Locate every blood parasite and identify its species.
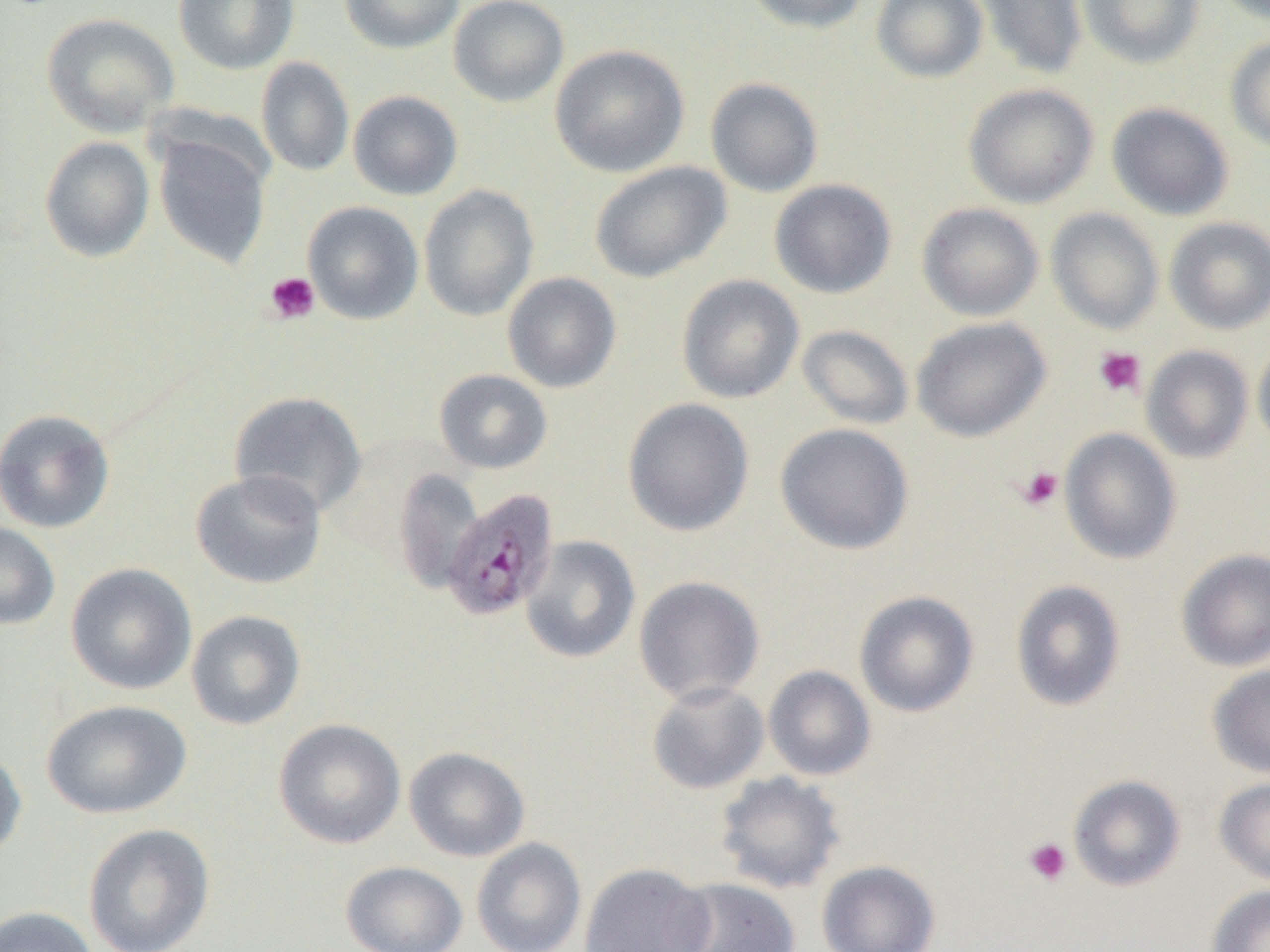

Approximate bounding boxes as named x1/y1/x2/y2 corners in pixels.
Plasmodium malariae-infected red blood cells: (x1=440, y1=487, x2=559, y2=622).
No Plasmodium falciparum, Plasmodium ovale, Plasmodium vivax, Babesia divergens, or Trypanosoma brucei observed.

Summary:
  - Uninfected red blood cell locations: (x1=173, y1=0, x2=299, y2=74), (x1=340, y1=0, x2=465, y2=54), (x1=448, y1=0, x2=569, y2=107), (x1=741, y1=0, x2=869, y2=34), (x1=871, y1=0, x2=988, y2=83), (x1=974, y1=0, x2=1089, y2=80), (x1=1078, y1=0, x2=1205, y2=68), (x1=1211, y1=0, x2=1269, y2=25), (x1=41, y1=12, x2=180, y2=137), (x1=1225, y1=36, x2=1270, y2=153), (x1=550, y1=44, x2=690, y2=178), (x1=256, y1=57, x2=355, y2=177), (x1=705, y1=77, x2=824, y2=198), (x1=963, y1=83, x2=1099, y2=209), (x1=348, y1=90, x2=463, y2=200), (x1=1106, y1=102, x2=1234, y2=221), (x1=153, y1=133, x2=271, y2=270), (x1=39, y1=136, x2=155, y2=263), (x1=589, y1=161, x2=732, y2=283), (x1=769, y1=179, x2=897, y2=299), (x1=419, y1=184, x2=539, y2=321), (x1=303, y1=201, x2=424, y2=325), (x1=917, y1=202, x2=1044, y2=321), (x1=1045, y1=208, x2=1164, y2=334), (x1=1164, y1=217, x2=1270, y2=334), (x1=502, y1=272, x2=622, y2=393), (x1=676, y1=274, x2=805, y2=404), (x1=911, y1=317, x2=1052, y2=442), (x1=797, y1=324, x2=915, y2=430), (x1=1252, y1=340, x2=1270, y2=453), (x1=1141, y1=345, x2=1254, y2=463), (x1=433, y1=368, x2=553, y2=474), (x1=228, y1=391, x2=368, y2=518), (x1=622, y1=397, x2=755, y2=536), (x1=0, y1=408, x2=116, y2=534), (x1=775, y1=423, x2=914, y2=554), (x1=1059, y1=428, x2=1181, y2=565), (x1=393, y1=468, x2=483, y2=592), (x1=190, y1=469, x2=327, y2=590), (x1=0, y1=521, x2=60, y2=630), (x1=520, y1=535, x2=641, y2=664), (x1=1176, y1=549, x2=1270, y2=672), (x1=65, y1=563, x2=197, y2=695), (x1=633, y1=575, x2=765, y2=705), (x1=1010, y1=579, x2=1127, y2=712), (x1=853, y1=590, x2=980, y2=717), (x1=186, y1=609, x2=306, y2=730), (x1=1207, y1=663, x2=1270, y2=778), (x1=763, y1=665, x2=876, y2=781), (x1=646, y1=680, x2=769, y2=794), (x1=41, y1=699, x2=192, y2=819), (x1=273, y1=718, x2=406, y2=849), (x1=404, y1=746, x2=530, y2=862), (x1=0, y1=747, x2=28, y2=864), (x1=715, y1=771, x2=846, y2=895), (x1=1067, y1=774, x2=1186, y2=891), (x1=1214, y1=776, x2=1270, y2=886), (x1=82, y1=822, x2=216, y2=952), (x1=471, y1=837, x2=587, y2=952), (x1=340, y1=860, x2=468, y2=952), (x1=816, y1=860, x2=940, y2=952), (x1=579, y1=862, x2=715, y2=952), (x1=666, y1=877, x2=800, y2=952), (x1=1205, y1=884, x2=1270, y2=952), (x1=0, y1=906, x2=99, y2=952)
  - Platelet locations: (x1=264, y1=272, x2=320, y2=324), (x1=1092, y1=346, x2=1146, y2=398), (x1=1016, y1=466, x2=1064, y2=511), (x1=1023, y1=837, x2=1072, y2=886)
  - Slide-level diagnosis: Plasmodium malariae
  - Field of view: single
  - Magnification: 1000x
  - Preparation: thin blood smear
  - Modality: optical microscopy
  - Image size: 1270×952 pixels